Locate every malaria parasite and identify its life-cycle stage.
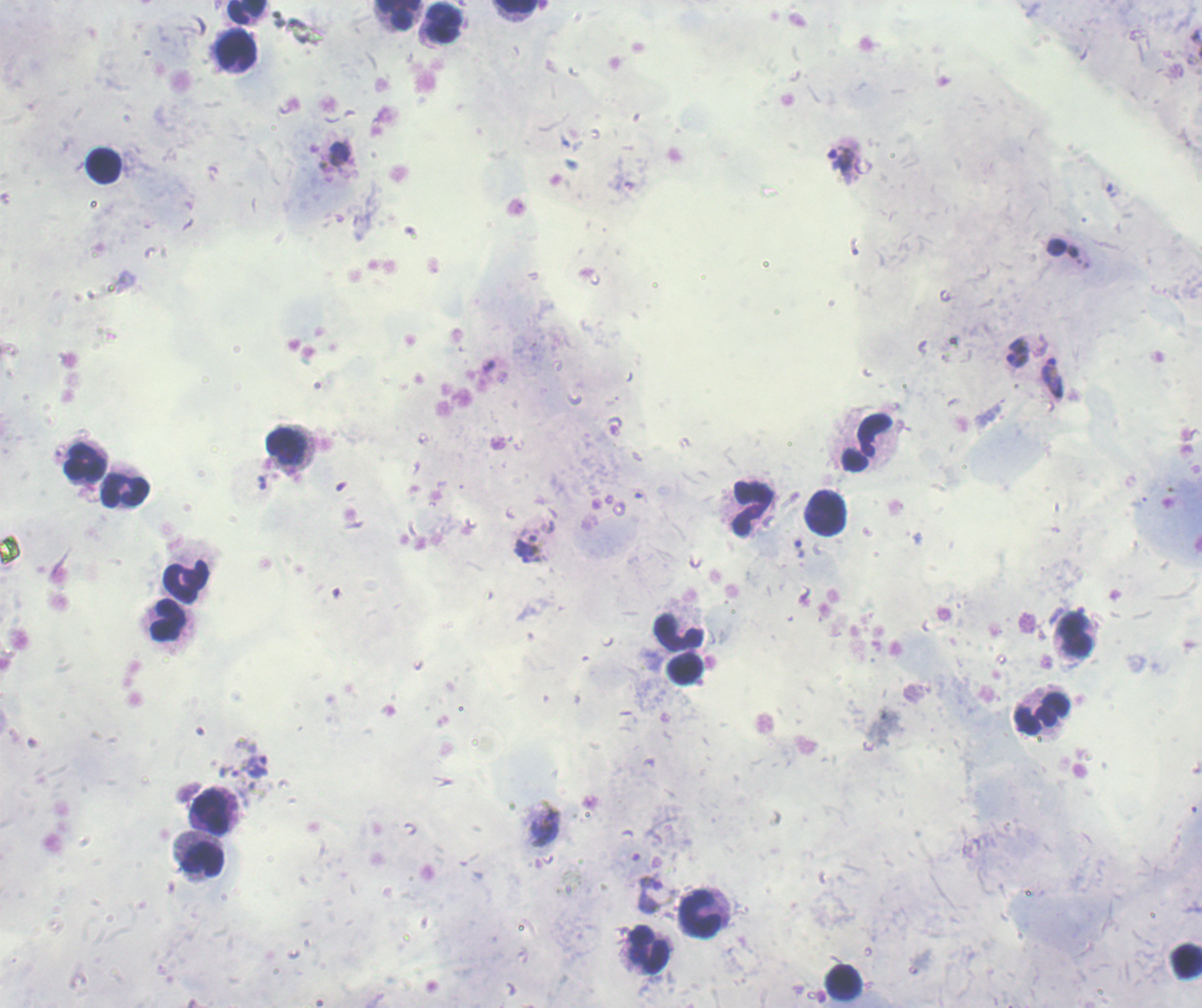
Approximate centers as (x, y) in pixels.
Trophozoites: (341, 154), (841, 164), (1018, 352), (1052, 378), (528, 548), (799, 548), (257, 766), (544, 825), (650, 896).
No schizont or gametocyte forms observed.

Approximate centers as (x, y) in pixels. Leukocyte locations: (246, 11), (517, 13), (398, 15), (443, 25), (236, 51), (103, 166), (867, 442), (287, 444), (83, 466), (124, 492), (752, 509), (826, 514), (189, 582), (168, 626), (678, 633), (1075, 637), (683, 670), (1041, 715), (213, 814), (202, 858), (701, 911), (648, 951), (1185, 959), (843, 982). 100x magnification. Romanowsky stain. Background quality: poor. Image is 1202×1008 pixels. Single field of view. Previously used in an actual diagnosis. Thick blood smear.